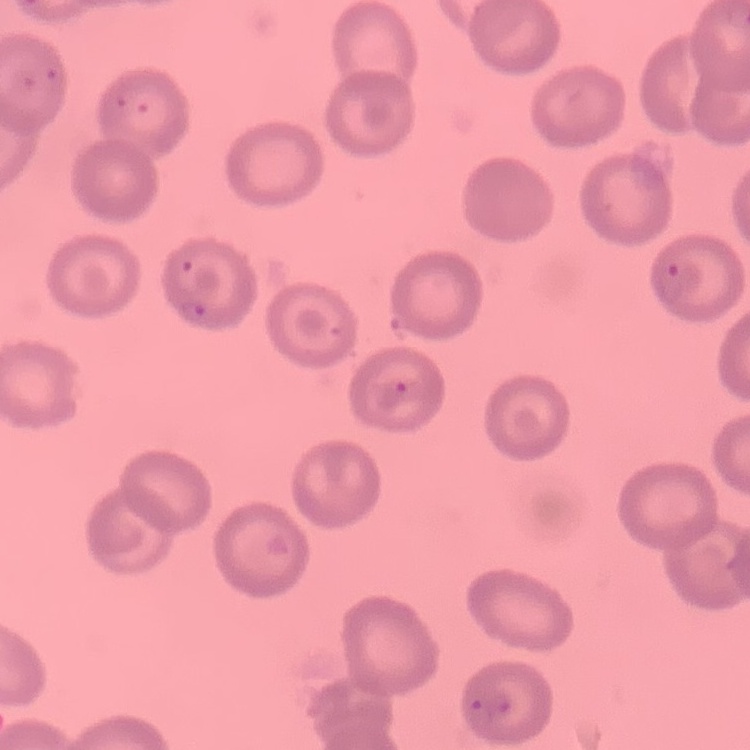
Summary:
  - Red blood cell morphology: no rouleaux formation
  - Image type: square crop of a larger photomicrograph
  - Preparation: thin peripheral smear
  - Stain: Field's or Giemsa